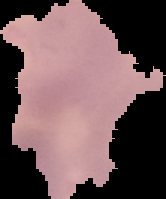
Malaria status: parasitized. The area outside the segmented cell region is set to black. From a thin blood film. Image is 166×199 pixels.